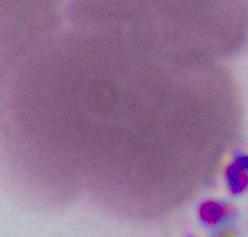

modality: photomicrograph
magnification: 1000x
identification: red blood cell